Classify this cell by malaria status.
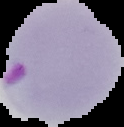

It is parasitized.

From a thin blood smear. Segmented cell region on a black background. Image is 124×127 pixels.